Classify this cell by malaria status.
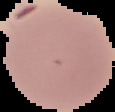
It is uninfected.

Summary:
  - Image type: cell region segmented out of the field of view; surrounding area masked to black
  - Preparation: thin blood film
  - Image size: 115×112 pixels